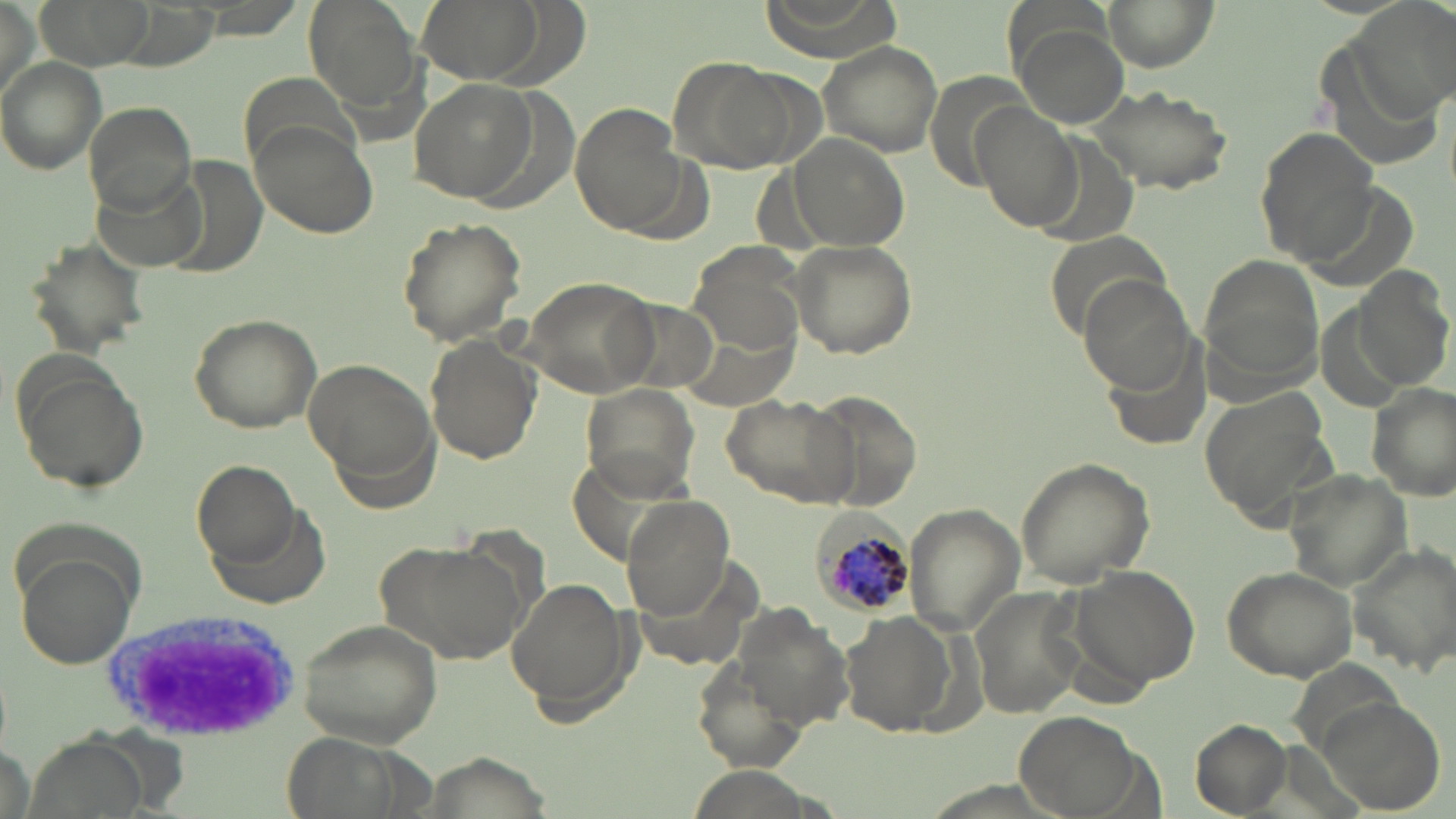
slide-level diagnosis = Plasmodium malariae
uninfected red blood cell locations = approximate bounding boxes as named x1/y1/x2/y2 corners in pixels: (x1=39, y1=0, x2=152, y2=66), (x1=304, y1=0, x2=421, y2=112), (x1=424, y1=0, x2=545, y2=82), (x1=758, y1=0, x2=899, y2=55), (x1=1100, y1=0, x2=1216, y2=70), (x1=1358, y1=0, x2=1456, y2=114), (x1=1014, y1=22, x2=1128, y2=127), (x1=815, y1=38, x2=946, y2=157), (x1=0, y1=56, x2=106, y2=174), (x1=669, y1=56, x2=806, y2=175), (x1=240, y1=77, x2=359, y2=163), (x1=410, y1=78, x2=539, y2=206), (x1=1086, y1=84, x2=1235, y2=195), (x1=84, y1=100, x2=197, y2=215), (x1=569, y1=102, x2=690, y2=236), (x1=974, y1=104, x2=1083, y2=231), (x1=247, y1=119, x2=377, y2=240), (x1=1252, y1=124, x2=1381, y2=261), (x1=790, y1=133, x2=911, y2=254), (x1=395, y1=215, x2=529, y2=347), (x1=23, y1=235, x2=151, y2=358), (x1=787, y1=238, x2=918, y2=359), (x1=687, y1=241, x2=807, y2=359), (x1=1201, y1=258, x2=1329, y2=388), (x1=1352, y1=264, x2=1454, y2=392), (x1=1079, y1=272, x2=1200, y2=396), (x1=521, y1=275, x2=662, y2=397), (x1=185, y1=311, x2=324, y2=433), (x1=681, y1=314, x2=798, y2=411), (x1=422, y1=335, x2=540, y2=465), (x1=8, y1=353, x2=151, y2=497), (x1=303, y1=357, x2=439, y2=492), (x1=579, y1=381, x2=700, y2=501), (x1=1367, y1=382, x2=1454, y2=498), (x1=1198, y1=389, x2=1335, y2=533), (x1=806, y1=390, x2=925, y2=514), (x1=718, y1=393, x2=858, y2=509), (x1=1013, y1=457, x2=1155, y2=588), (x1=191, y1=459, x2=299, y2=561), (x1=1284, y1=470, x2=1415, y2=590), (x1=622, y1=496, x2=734, y2=617), (x1=903, y1=502, x2=1025, y2=633), (x1=373, y1=538, x2=528, y2=668), (x1=1350, y1=541, x2=1455, y2=672), (x1=15, y1=556, x2=138, y2=670), (x1=1071, y1=564, x2=1202, y2=689), (x1=1221, y1=567, x2=1357, y2=681), (x1=507, y1=575, x2=633, y2=717), (x1=971, y1=588, x2=1085, y2=721), (x1=738, y1=608, x2=855, y2=732), (x1=842, y1=612, x2=956, y2=736), (x1=294, y1=617, x2=444, y2=748), (x1=690, y1=659, x2=810, y2=774), (x1=1322, y1=699, x2=1443, y2=816), (x1=1011, y1=707, x2=1148, y2=815), (x1=1186, y1=719, x2=1294, y2=817), (x1=23, y1=732, x2=151, y2=819)
image size = 1456×819 pixels
Plasmodium malariae-infected red blood cell locations = approximate bounding boxes as named x1/y1/x2/y2 corners in pixels: (x1=807, y1=508, x2=917, y2=620)
white blood cell locations = approximate bounding boxes as named x1/y1/x2/y2 corners in pixels: (x1=113, y1=601, x2=303, y2=737)
field of view = single
magnification = 1000x
preparation = thin blood smear
stain = May-Grünwald-Giemsa
modality = light microscopy